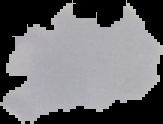

From a thin blood smear. The area outside the segmented cell region is set to black. Image is 163×124 pixels. Malaria status: parasitized.